State which cell type is depicted.
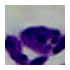

This is a leukocyte.

Summary:
  - Magnification: 1000x
  - Modality: micrograph